Assess this cell for malaria.
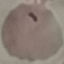
It is parasitized.

stain: Giemsa
image_type: cell patch, automatically extracted from a larger field of view and resized to 64 × 64 pixels
capture: smartphone camera at the microscope eyepiece
preparation: thin smear